Identify the parasite.
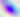

This is Toxoplasma gondii.

Summary:
  - Modality: photomicrograph
  - Magnification: 400x